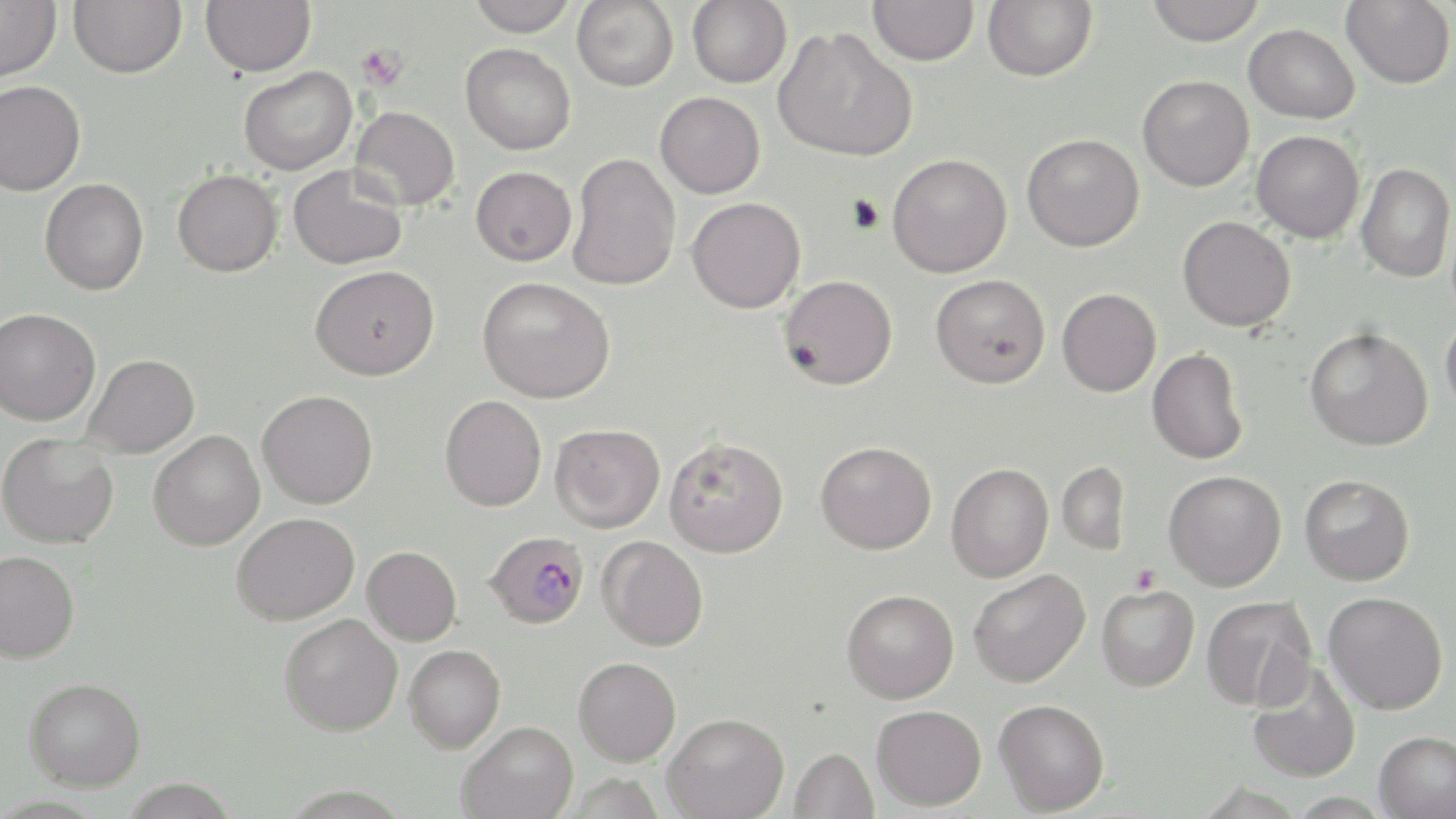 Approximate bounding boxes as (x1,y1)-(x2,y2) corner pairs in pixels. Uninfected red blood cell locations: (0,0)-(61,82), (68,0)-(187,78), (200,0)-(315,76), (466,0)-(577,37), (572,0)-(678,92), (687,0)-(792,87), (868,0)-(978,66), (983,0)-(1097,81), (1145,0)-(1265,45), (1341,0)-(1455,88), (1243,24)-(1359,123), (773,25)-(917,162), (460,43)-(576,155), (238,66)-(356,176), (1137,75)-(1254,191), (0,81)-(86,196), (655,91)-(765,199), (351,105)-(460,210), (1252,130)-(1364,242), (1021,133)-(1144,252), (568,153)-(681,291), (887,154)-(1012,278), (1356,163)-(1455,283), (288,165)-(408,270), (471,166)-(576,266), (172,169)-(282,277), (40,178)-(149,295), (687,197)-(806,313), (1178,216)-(1296,331), (310,265)-(440,380), (930,274)-(1050,388), (779,275)-(897,390), (477,277)-(616,404), (1057,288)-(1161,396), (0,308)-(101,426), (1440,312)-(1456,419), (1304,327)-(1433,450), (1147,349)-(1248,464), (83,354)-(199,458), (257,389)-(378,508), (440,395)-(547,511), (550,423)-(665,533), (149,430)-(266,551), (0,434)-(119,549), (664,437)-(789,557), (815,441)-(937,554), (1057,461)-(1130,555), (946,463)-(1053,582), (1164,470)-(1287,591), (1299,474)-(1415,586), (232,512)-(359,625), (598,536)-(709,651), (362,546)-(462,645), (0,550)-(80,663), (969,569)-(1090,687), (1097,584)-(1199,691), (842,589)-(959,703), (1324,591)-(1448,714), (1202,595)-(1317,711), (279,614)-(403,736), (404,644)-(506,752), (573,657)-(681,766), (1247,663)-(1361,783), (24,677)-(146,791), (994,698)-(1109,815), (871,704)-(986,810), (663,712)-(789,818), (457,721)-(578,818), (1374,730)-(1455,819), (790,747)-(879,818). Platelet locations: (356,44)-(408,91), (1129,564)-(1161,594). Plasmodium falciparum-infected red blood cell locations: (484,531)-(590,629). Slide-level diagnosis: Plasmodium falciparum. May-Grünwald-Giemsa-stained preparation. Thin blood film. Image is 1456×819 pixels. Captured at 1000x magnification. Single field of view. Light microscopy.